Identify the cell.
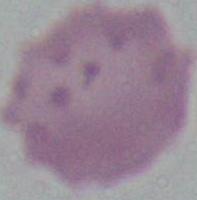
This is an erythrocyte.

Micrograph. Captured at 1000x magnification.